Evaluate for malaria.
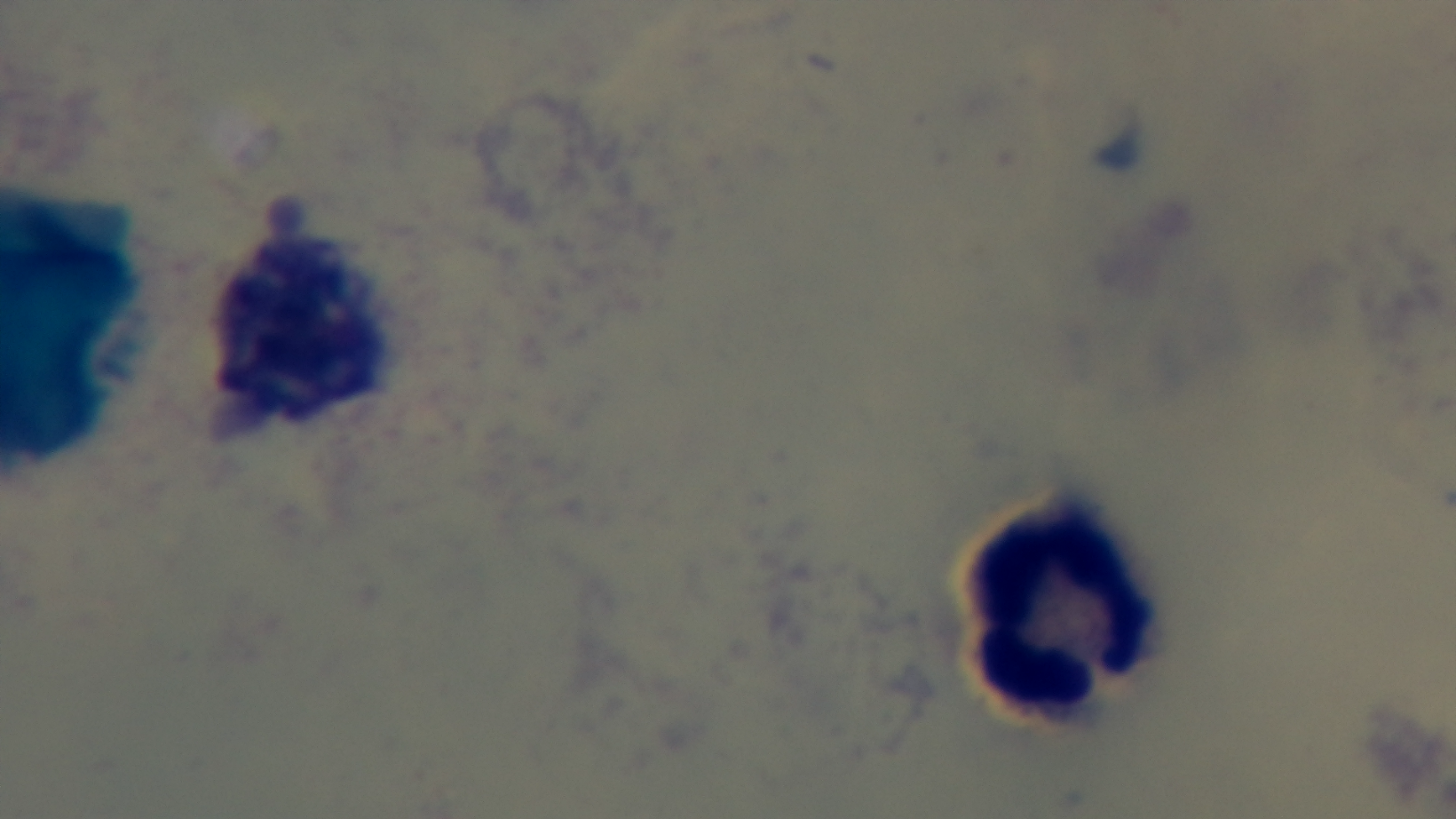

It is uninfected.

Summary:
  - Preparation: thick blood film
  - Modality: light microscopy
  - Capture: mounted 4K digital camera
  - Objective: 100x oil immersion
  - Stain: Giemsa
  - Field of view: one from the slide